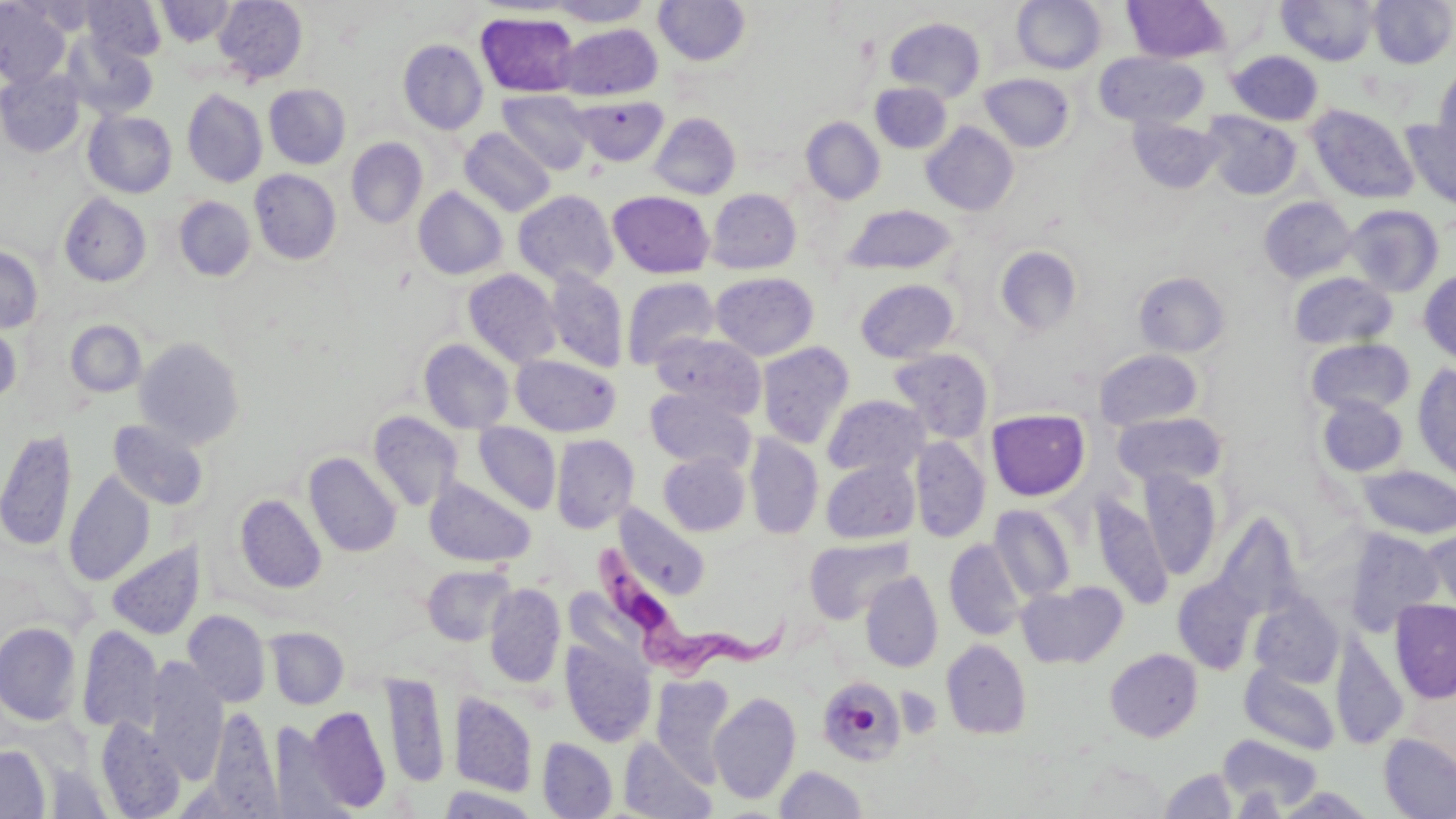

Approximate bounding boxes as (x1,y1)-(x2,y2) corner pairs in pixels. Uninfected red blood cell locations: (82,0)-(166,62), (214,0)-(308,84), (546,0)-(654,26), (1012,0)-(1107,74), (1123,0)-(1228,63), (1277,0)-(1379,66), (1368,0)-(1456,68), (0,1)-(70,88), (156,1)-(235,46), (654,1)-(750,66), (476,12)-(580,97), (884,18)-(986,102), (557,24)-(662,100), (61,32)-(158,120), (398,40)-(488,134), (1227,50)-(1324,125), (1095,52)-(1208,128), (1432,64)-(1456,167), (0,68)-(84,157), (978,73)-(1075,153), (871,82)-(951,154), (264,84)-(350,169), (182,89)-(267,187), (497,90)-(594,174), (573,95)-(668,166), (1306,104)-(1419,205), (83,111)-(177,198), (1202,111)-(1302,200), (649,112)-(741,199), (1128,116)-(1224,194), (801,117)-(885,204), (1402,120)-(1456,213), (921,122)-(1018,215), (459,127)-(555,216), (346,138)-(428,228), (249,169)-(341,264), (413,187)-(507,279), (706,188)-(801,274), (513,190)-(618,286), (608,191)-(715,278), (59,193)-(151,287), (174,196)-(255,281), (1259,197)-(1356,283), (1343,204)-(1444,297), (844,205)-(957,275), (0,245)-(43,333), (994,245)-(1083,337), (463,269)-(562,368), (544,269)-(629,372), (1418,269)-(1456,366), (1133,271)-(1230,357), (710,272)-(819,360), (1288,272)-(1398,350), (621,277)-(720,369), (855,279)-(959,363), (0,320)-(22,406), (65,320)-(146,397), (649,331)-(766,419), (135,337)-(245,449), (1306,338)-(1415,417), (419,339)-(514,433), (756,341)-(855,449), (887,347)-(994,444), (1094,348)-(1204,430), (511,355)-(621,436), (1411,363)-(1456,480), (646,388)-(756,473), (822,395)-(930,478), (1316,395)-(1408,477), (986,409)-(1090,500), (368,411)-(463,512), (1113,412)-(1227,488), (108,420)-(208,511), (473,422)-(561,513), (0,428)-(77,552), (550,434)-(639,533), (745,434)-(823,539), (910,436)-(990,543), (304,452)-(401,557), (658,452)-(750,536), (820,458)-(920,544), (1357,465)-(1456,539), (1137,468)-(1222,580), (64,470)-(156,586), (425,478)-(535,567), (1090,493)-(1172,608), (235,494)-(326,593), (614,505)-(711,600), (989,505)-(1076,602), (1213,512)-(1303,620), (1422,524)-(1456,619), (1342,528)-(1445,635), (804,536)-(912,624), (944,539)-(1027,641), (107,542)-(204,640), (421,564)-(514,646), (861,571)-(943,672), (1172,576)-(1258,673), (1017,580)-(1128,668), (484,583)-(565,688), (1249,591)-(1344,688), (1390,599)-(1456,703), (182,609)-(271,708), (0,622)-(81,725), (76,624)-(163,735), (264,627)-(349,709), (560,637)-(656,747), (941,639)-(1032,739), (1331,640)-(1408,750), (1105,648)-(1203,741), (145,658)-(228,782), (1241,663)-(1340,754), (380,671)-(450,788), (652,675)-(734,783), (816,677)-(907,767), (449,691)-(538,797), (709,692)-(801,804), (303,706)-(391,812), (206,707)-(280,813), (95,717)-(185,818), (1378,732)-(1456,819), (1219,733)-(1322,812), (619,736)-(717,819), (537,737)-(617,818), (0,745)-(51,819), (775,765)-(868,818), (1160,768)-(1238,818), (436,786)-(541,818). Trypanosoma brucei locations: (590,538)-(787,690). Slide-level diagnosis: Trypanosoma brucei. Image is 1456×819 pixels. Captured at 1000x magnification. May-Grünwald-Giemsa-stained preparation. Single field of view. Optical microscopy. Thin blood smear.